State which parasite is depicted.
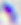

This is Toxoplasma gondii.

Summary:
  - Magnification: 400x
  - Modality: micrograph